Name the parasite shown.
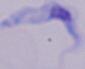

This is a trypanosome.

Summary:
  - Modality: photomicrograph
  - Magnification: 1000x